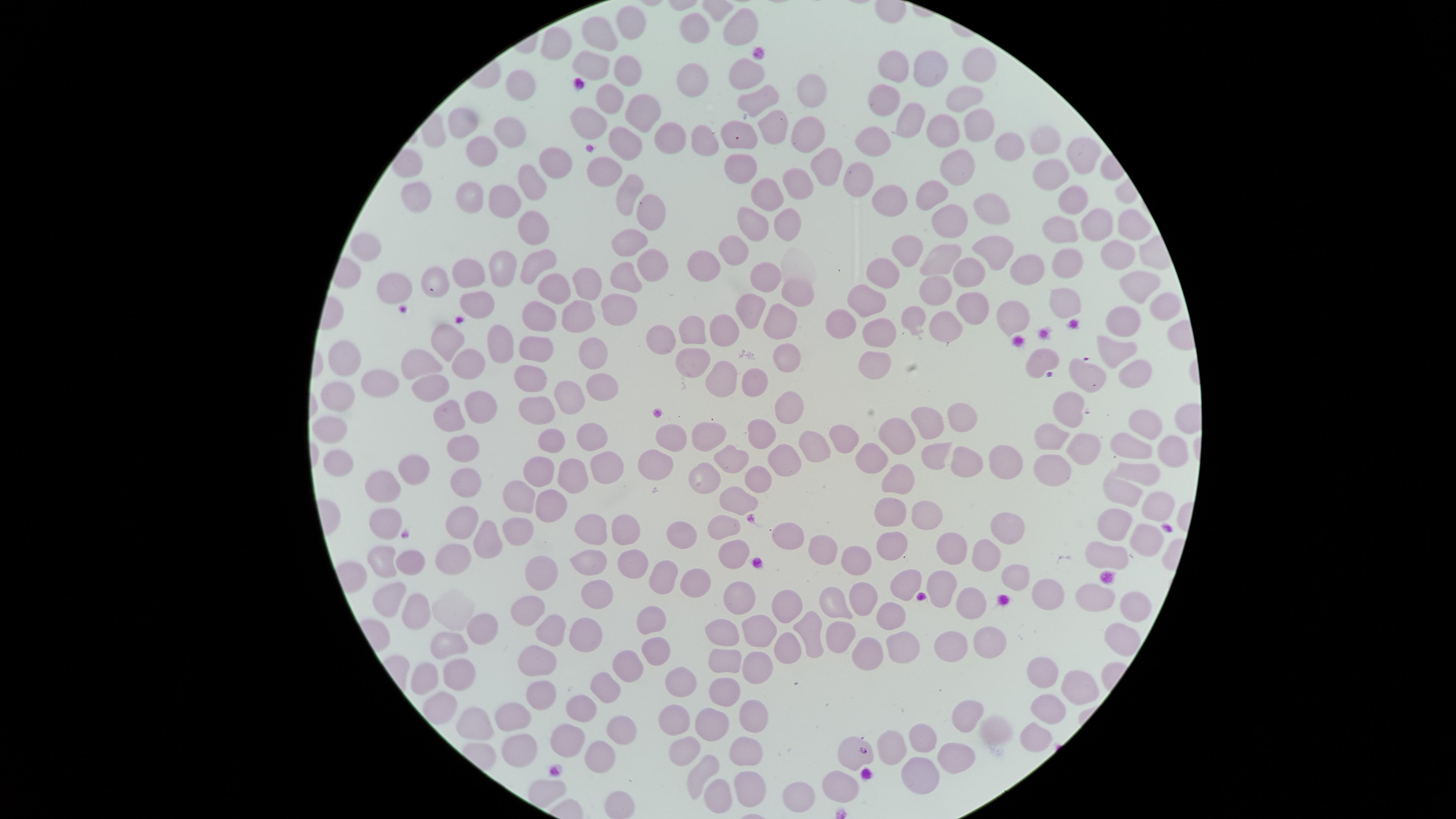
Approximate marker points as (x, y) in pixels.
Summary:
  - Uninfected red blood cells: (628, 17), (742, 25), (688, 27), (600, 36), (553, 46), (976, 62), (590, 63), (898, 65), (937, 65), (625, 68), (746, 69), (693, 76), (519, 85), (966, 90), (813, 92), (882, 93), (762, 98), (610, 100), (640, 107), (465, 115), (586, 118), (907, 118), (773, 121), (940, 126), (981, 127), (514, 129), (801, 129), (668, 134), (701, 136), (1045, 137), (740, 140), (877, 141), (624, 145), (1014, 145), (481, 149), (1084, 151), (552, 157), (822, 160), (948, 167), (603, 168), (741, 168), (1053, 172), (856, 178), (524, 180), (795, 180), (929, 187), (623, 191), (770, 191), (468, 193), (413, 195), (890, 199), (1072, 199), (992, 201), (501, 202), (645, 212), (783, 217), (953, 218), (1129, 220), (1094, 221), (745, 225), (536, 226), (1067, 230), (628, 239), (367, 241), (733, 248), (909, 249), (1118, 250), (997, 252), (542, 256), (942, 256), (649, 259), (1064, 264), (700, 265), (503, 267), (1031, 267), (877, 268), (627, 272), (968, 273), (467, 277), (767, 278), (582, 279), (395, 282), (436, 282), (1136, 283), (791, 288), (932, 288), (548, 289), (620, 298), (864, 298), (1064, 299), (1164, 299), (481, 301), (974, 303), (754, 305), (578, 315), (1009, 315), (539, 316), (909, 316), (779, 322), (1124, 324), (841, 328), (943, 328), (718, 332), (882, 332), (668, 334), (687, 335), (443, 338), (503, 345), (533, 350), (1117, 350), (594, 351), (788, 353), (877, 357), (348, 359), (692, 359), (466, 360), (427, 362), (1045, 362), (1129, 372), (719, 375), (1094, 376), (528, 381), (603, 381), (380, 382), (754, 382), (430, 388), (337, 393), (569, 398), (477, 403), (789, 403), (534, 408), (1065, 408), (932, 413), (1142, 414), (443, 415), (961, 421), (329, 426), (767, 426), (710, 433), (585, 435), (1047, 435), (899, 436), (668, 438), (841, 438), (553, 440), (1134, 441), (459, 443), (816, 443), (1079, 446), (1167, 448), (778, 452), (932, 452), (337, 454), (873, 455), (1008, 456), (967, 459), (652, 463), (733, 463), (1048, 465), (538, 468), (606, 469), (408, 470), (1137, 473), (702, 474), (568, 476), (900, 477), (754, 478), (463, 480), (379, 486), (1122, 492), (522, 495), (732, 498), (550, 501), (1153, 506), (931, 509), (888, 515), (460, 520), (518, 522), (382, 525), (714, 525), (1113, 525), (590, 527), (625, 527), (1006, 528), (782, 532), (1140, 532), (688, 536), (486, 539), (888, 545), (819, 548), (949, 548), (734, 549), (1106, 553), (448, 555), (852, 556), (980, 556), (373, 558), (410, 562), (587, 563), (633, 566), (539, 575), (656, 575), (1015, 575), (690, 577), (942, 582), (904, 583), (1092, 590), (591, 593), (1050, 593), (857, 594), (388, 597), (741, 601), (782, 601), (831, 602), (965, 602), (1122, 604), (526, 607), (414, 608), (889, 618), (643, 621), (481, 628), (550, 629), (805, 630), (755, 631), (835, 634), (583, 635), (714, 635), (1113, 635), (992, 639), (448, 643), (949, 645), (655, 646), (774, 647), (900, 649), (866, 651), (545, 657), (721, 659), (623, 668), (425, 672), (455, 673), (753, 677), (1037, 677), (682, 680), (1073, 686), (600, 687), (537, 691), (721, 694), (431, 701), (581, 705), (673, 711), (1047, 711), (965, 712), (466, 714), (748, 717), (506, 718), (704, 721), (619, 723), (996, 731), (1031, 733), (921, 736), (892, 739), (743, 742), (509, 745), (562, 747), (682, 749), (848, 751), (954, 751), (592, 752), (701, 765), (747, 778), (910, 778), (838, 784), (710, 791), (795, 791), (618, 805)
  - Presence: no malaria parasites detected
  - Preparation: thin smear of blood
  - Capture: smartphone photograph through the microscope eyepiece
  - Stain: Giemsa
  - Visible region: circular
  - Image size: 1456×819 pixels
  - Field of view: single